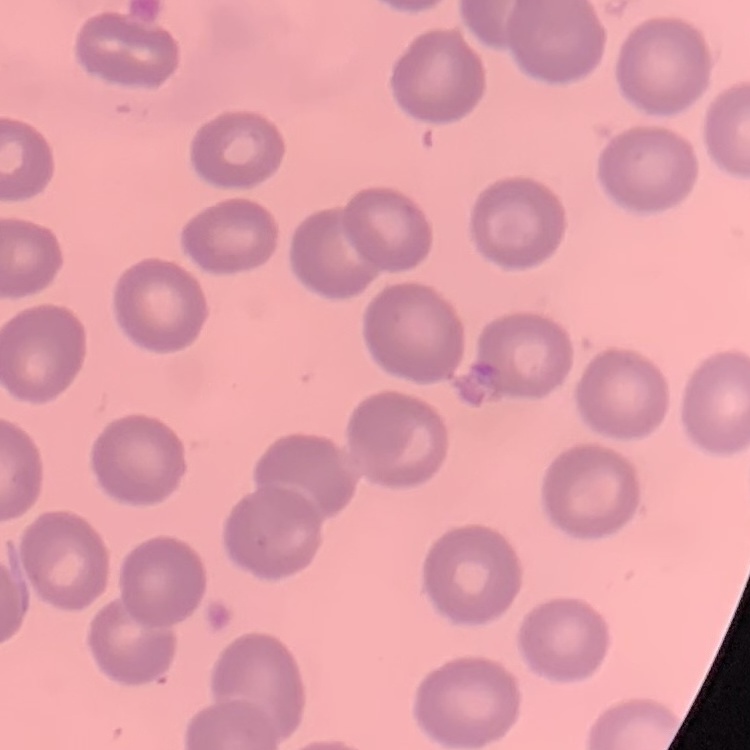
Summary:
  - Red blood cell morphology: no rouleaux formation
  - Image type: square crop of a larger photomicrograph
  - Stain: Field's or Giemsa
  - Preparation: thin peripheral smear